Identify the parasite.
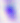
This is Toxoplasma gondii.

Photomicrograph. 400x magnification.